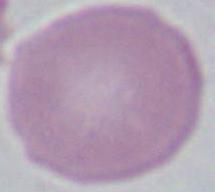

A red blood cell is seen. Photomicrograph. Captured at 1000x magnification.